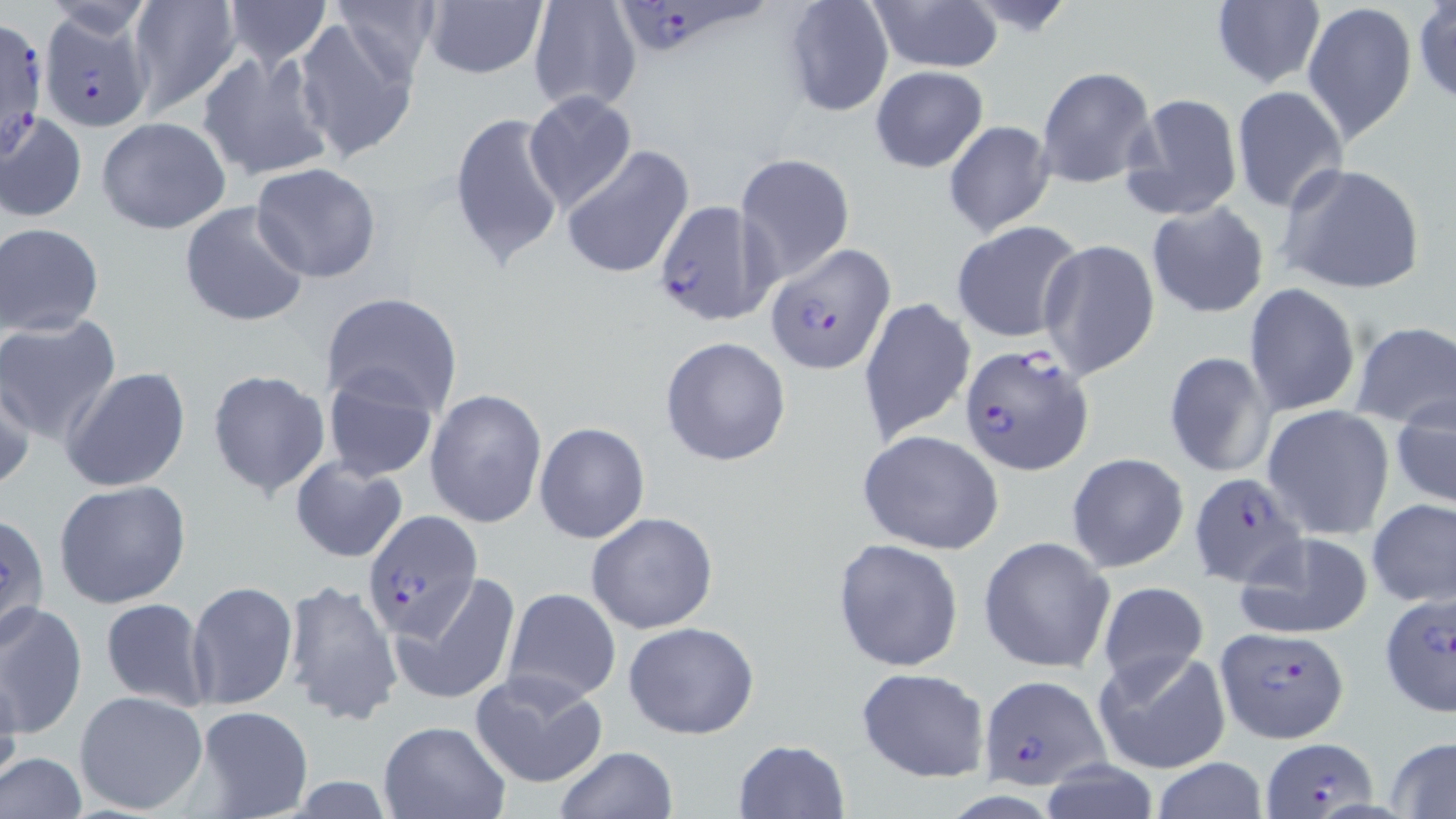

Summary:
  - Coordinate format: approximate bounding boxes as (x1,y1)-(x2,y2) corner pairs in pixels
  - Uninfected red blood cell locations: (123,0)-(241,116), (220,0)-(334,66), (330,0)-(442,81), (526,0)-(643,116), (1210,0)-(1325,89), (869,1)-(1002,73), (1301,1)-(1416,147), (421,2)-(549,80), (781,2)-(894,117), (1413,2)-(1456,107), (292,17)-(420,164), (272,41)-(408,267), (194,51)-(334,183), (1035,64)-(1158,190), (869,65)-(988,172), (1231,86)-(1348,212), (524,90)-(637,213), (1122,91)-(1244,222), (2,109)-(88,224), (449,111)-(565,268), (97,117)-(232,235), (943,120)-(1057,238), (560,145)-(694,281), (736,153)-(855,287), (1274,162)-(1428,294), (250,163)-(381,283), (178,199)-(311,329), (1146,201)-(1270,319), (951,220)-(1084,343), (1,222)-(104,338), (1039,238)-(1161,380), (1244,284)-(1361,417), (318,292)-(462,418), (857,297)-(975,444), (0,316)-(122,444), (1350,320)-(1456,430), (660,336)-(792,468), (1163,350)-(1275,479), (62,366)-(192,492), (0,368)-(35,494), (205,369)-(330,501), (319,371)-(440,483), (425,389)-(547,527), (1391,391)-(1456,511), (1263,405)-(1395,540), (533,421)-(651,544), (858,430)-(1005,555), (1066,453)-(1190,574), (291,454)-(409,564), (53,481)-(192,611), (1367,500)-(1456,606), (1,512)-(50,645), (585,512)-(718,634), (1230,531)-(1375,641), (977,535)-(1114,674), (832,538)-(965,671), (393,572)-(524,708), (280,580)-(401,729), (186,581)-(299,710), (1096,581)-(1208,689), (502,587)-(622,706), (98,596)-(213,711), (0,601)-(87,742), (623,620)-(759,740), (1091,649)-(1231,776), (467,667)-(610,789), (0,668)-(24,789), (855,668)-(989,782), (74,690)-(209,816), (192,707)-(314,818), (376,719)-(513,818), (1386,736)-(1456,818), (734,739)-(849,817), (553,746)-(677,819), (1,752)-(87,819), (1150,758)-(1271,818), (1037,761)-(1164,819)
  - Plasmodium falciparum-infected red blood cell locations: (622,0)-(768,58), (39,7)-(155,132), (0,19)-(49,164), (653,200)-(772,325), (763,244)-(894,374), (960,342)-(1097,475), (1188,472)-(1308,589), (362,512)-(485,640), (1377,592)-(1456,717), (1216,626)-(1349,744), (976,674)-(1110,790), (1263,738)-(1381,817)
  - Slide-level diagnosis: Plasmodium falciparum
  - Magnification: 1000x
  - Modality: optical microscopy
  - Image size: 1456×819 pixels
  - Field of view: single
  - Stain: May-Grünwald-Giemsa
  - Preparation: thin blood film